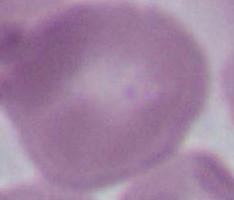

Summary:
  - Magnification: 1000x
  - Identification: erythrocyte
  - Modality: micrograph